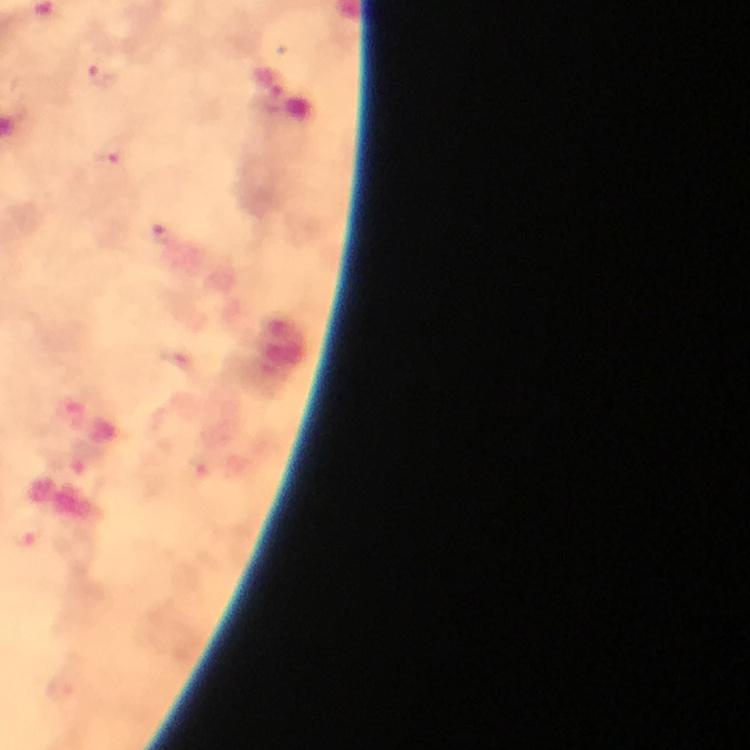
Approximate object centers, in pixels from the top-left corner. Plasmodium parasite locations: (x=103, y=76), (x=110, y=165), (x=164, y=236). From a diagnostic examination for malaria. Immersion oil was used. Thick smear. Giemsa-stained preparation. Image is 750×750 pixels. 100x magnification. Photographed with a smartphone mounted on the microscope. A crop from one field of view.